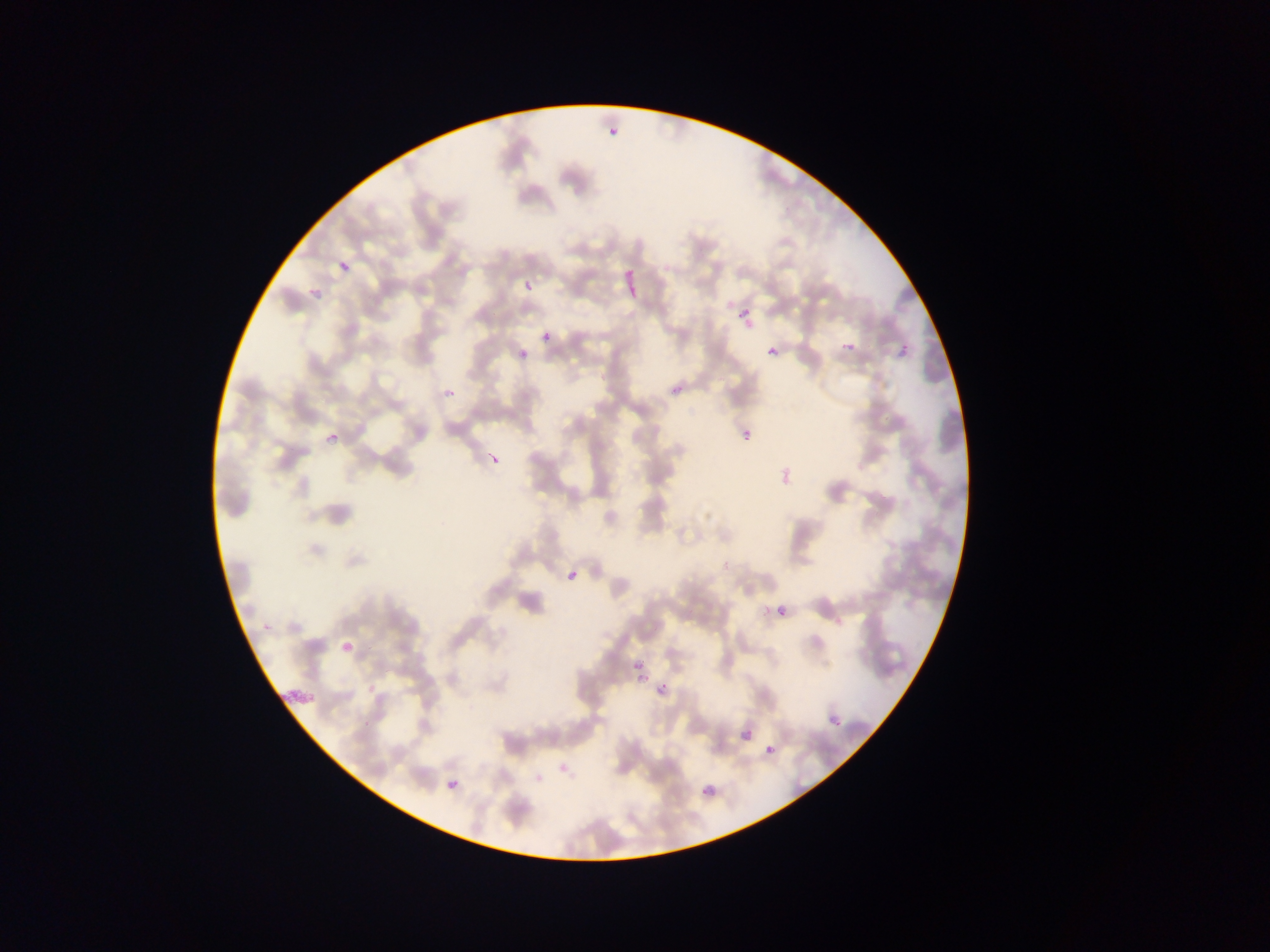

Approximate bounding boxes as {left, top, right, bottom} in pixels.
Summary:
  - Plasmodium parasite locations: {607, 121, 619, 143}, {336, 254, 352, 271}, {524, 281, 533, 290}, {304, 289, 326, 299}, {732, 307, 750, 325}, {541, 332, 551, 342}, {836, 337, 864, 357}, {894, 337, 913, 362}, {515, 346, 528, 360}, {767, 346, 779, 357}, {666, 375, 694, 395}, {442, 389, 454, 403}, {743, 430, 752, 440}, {325, 434, 332, 447}, {486, 453, 499, 470}, {777, 459, 793, 483}, {562, 567, 582, 586}, {762, 605, 770, 615}, {777, 606, 786, 616}, {337, 616, 364, 658}, {630, 652, 644, 672}, {632, 673, 646, 689}, {653, 678, 674, 707}, {828, 714, 841, 727}, {741, 729, 752, 741}, {765, 744, 775, 755}, {446, 778, 458, 790}, {701, 788, 709, 795}
  - Field of view: single
  - Image size: 1270×952 pixels
  - Preparation: thin blood film
  - Capture: mobile-phone photograph through a microscope
  - Country: Ghana